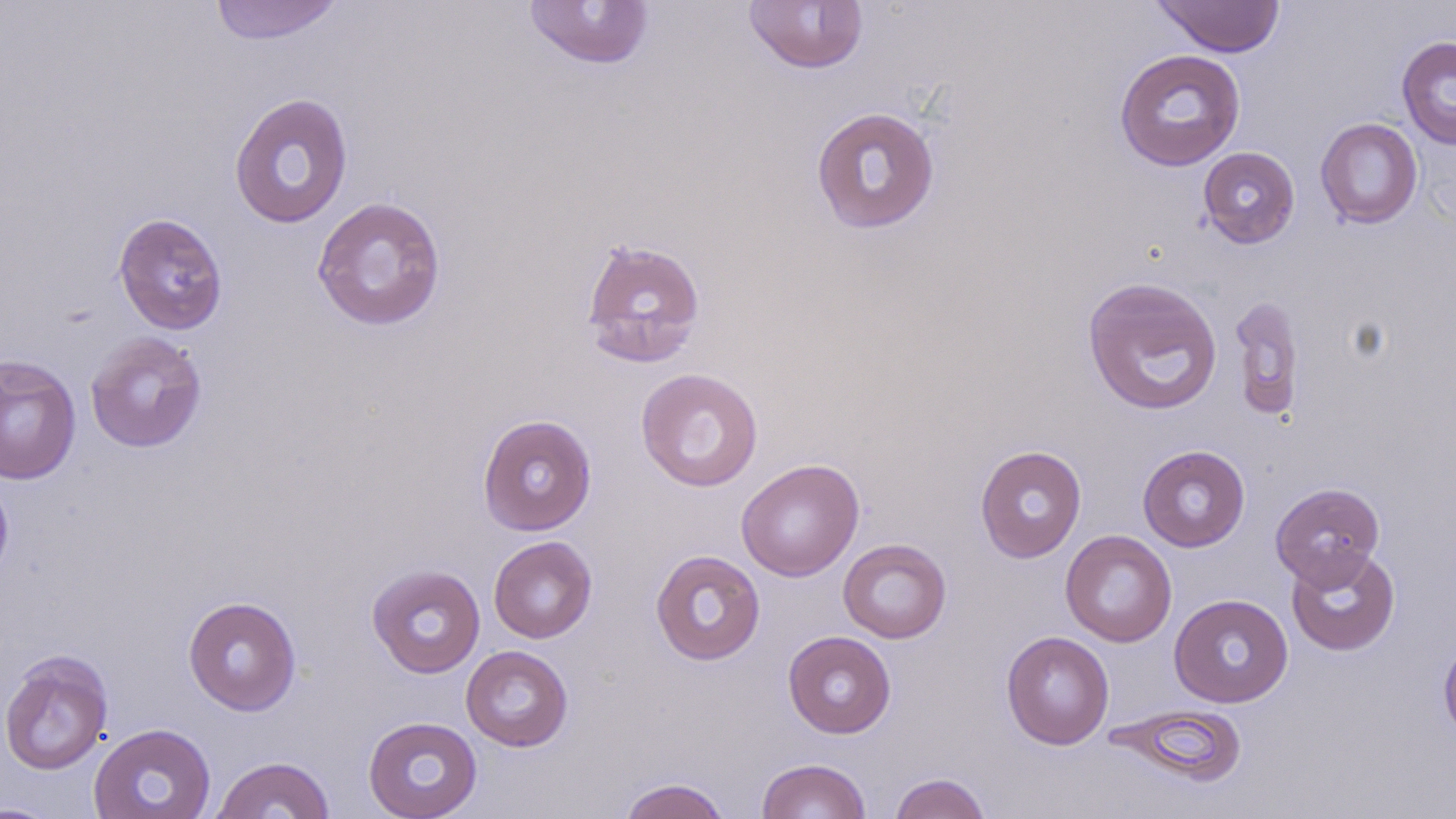
Summary:
  - Coordinate format: approximate bounding boxes as (x1, y1, x2, y2) in pixels
  - Uninfected red blood cell locations: (207, 0, 347, 45), (742, 0, 870, 74), (521, 1, 655, 70), (1152, 1, 1286, 57), (1396, 35, 1456, 150), (1114, 49, 1246, 171), (228, 92, 354, 229), (810, 106, 941, 235), (1315, 117, 1423, 229), (1197, 146, 1300, 249), (312, 196, 447, 331), (113, 212, 228, 335), (579, 237, 707, 370), (1082, 276, 1223, 417), (1229, 294, 1306, 422), (85, 332, 207, 453), (0, 355, 81, 485), (636, 368, 763, 491), (477, 413, 597, 536), (975, 445, 1086, 562), (1137, 445, 1250, 552), (736, 459, 864, 581), (0, 469, 14, 587), (1270, 482, 1384, 588), (1060, 530, 1177, 647), (488, 535, 597, 643), (838, 538, 951, 643), (1286, 546, 1400, 656), (650, 550, 766, 665), (367, 564, 486, 679), (1169, 593, 1293, 708), (183, 595, 302, 715), (1001, 630, 1114, 749), (783, 631, 896, 738), (1438, 634, 1456, 746), (461, 645, 573, 751), (0, 649, 113, 776), (1106, 703, 1249, 788), (363, 716, 483, 818), (88, 723, 216, 819), (211, 755, 336, 818), (756, 758, 872, 819), (888, 772, 992, 819), (616, 777, 732, 819), (0, 801, 66, 818)
  - Slide-level diagnosis: negative for blood parasites
  - Magnification: 1000x
  - Modality: optical microscopy
  - Field of view: single
  - Image size: 1456×819 pixels
  - Stain: May-Grünwald-Giemsa
  - Preparation: thin blood smear